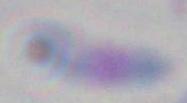 Captured at 1000x magnification. Toxoplasma gondii is shown. Micrograph.